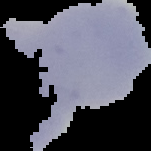

image_size: 151×151 pixels
image_type: segmented cell region with the area outside set to black
result: negative for malaria parasites
preparation: thin blood film